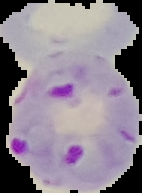 The area outside the segmented cell region is set to black. From a thin blood film. Result: Plasmodium parasites identified. Image is 142×193 pixels.